Point out each Plasmodium parasite.
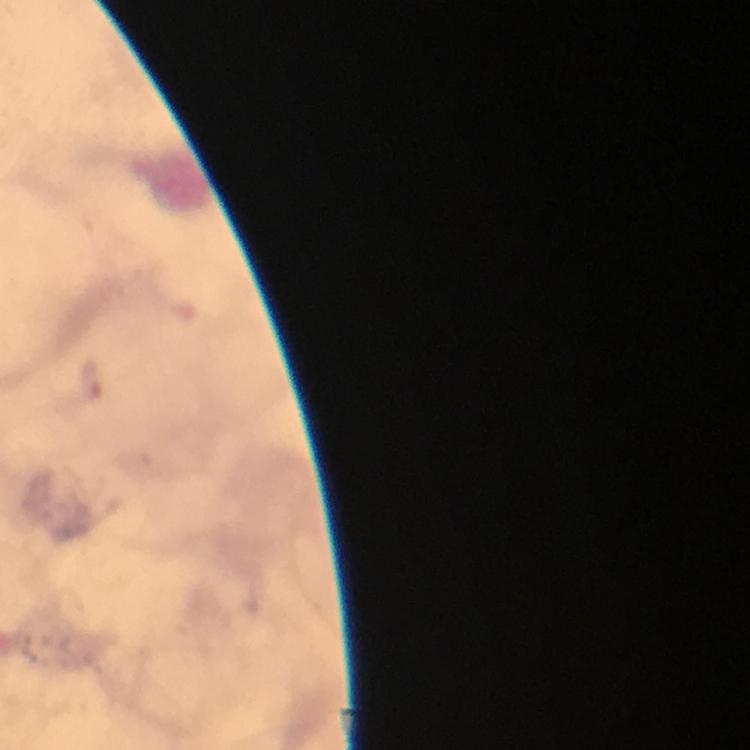

Approximate centers as (x, y) in pixels.
Plasmodium parasites: (92, 380).

Summary:
  - Capture: smartphone camera through the microscope
  - Magnification: 100x
  - Context: from a malaria diagnostic workup
  - Immersion oil: applied
  - Preparation: thick blood film
  - Image size: 750×750 pixels
  - Cropped from: a single field of view
  - Stain: Giemsa